Name the parasite shown.
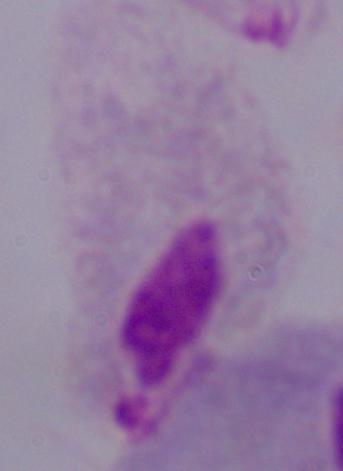
This is a trichomonad.

Photomicrograph. 1000x magnification.